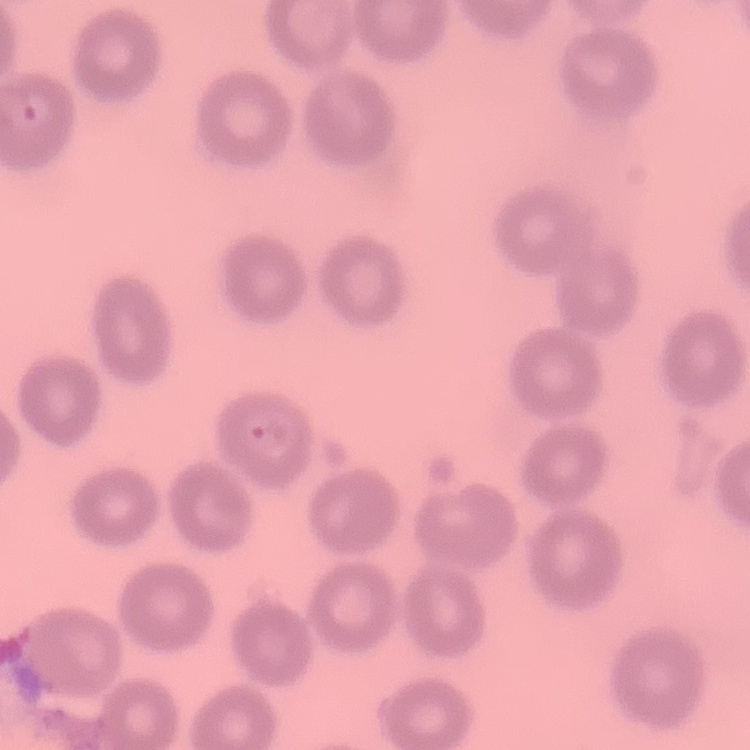

erythrocyte morphology = no rouleaux formation
stain = Field's or Giemsa
preparation = thin peripheral smear
image type = one tile cut from a larger photomicrograph